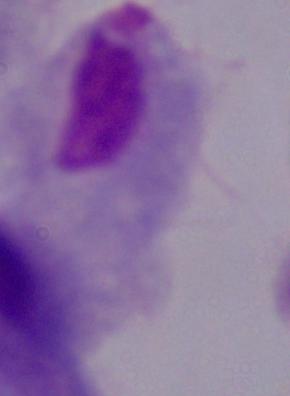
Summary:
  - Identification: trichomonad
  - Modality: micrograph
  - Magnification: 1000x